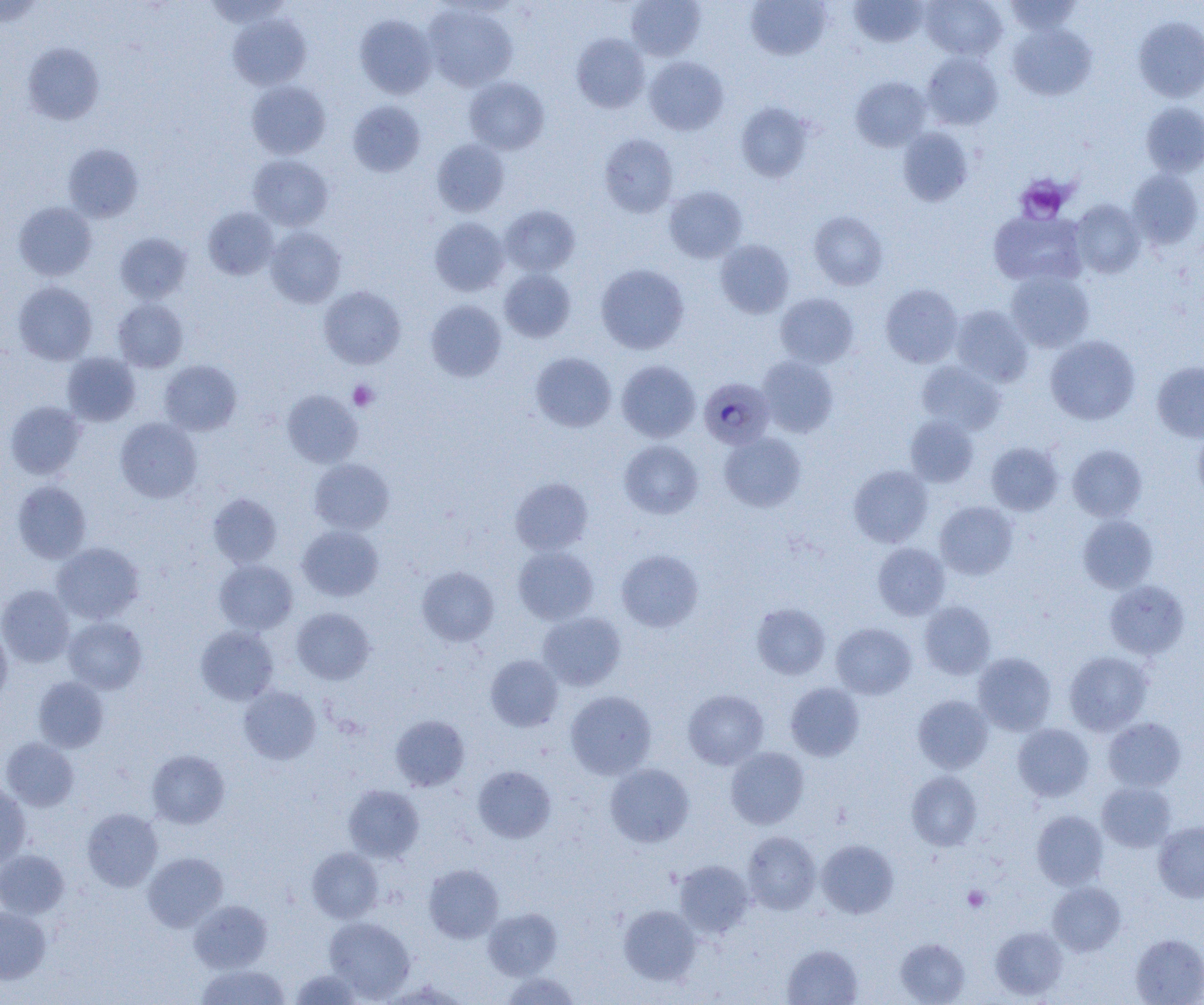
slide-level diagnosis = Plasmodium malariae
field of view = one of a larger specimen
image size = 1204×1005 pixels
magnification = 1000x
Plasmodium malariae-infected red blood cell locations = approximate bounding boxes as [x1, y1, x2, y2] in pixels: [699, 377, 775, 449]
modality = light microscopy
platelet locations = approximate bounding boxes as [x1, y1, x2, y2] in pixels: [1015, 174, 1073, 223], [348, 380, 378, 411], [962, 886, 990, 912]
preparation = thin blood smear
uninfected red blood cell locations = approximate bounding boxes as [x1, y1, x2, y2] in pixels: [626, 0, 706, 61], [849, 0, 927, 47], [921, 0, 1007, 60], [1004, 0, 1082, 34], [0, 1, 46, 27], [746, 1, 832, 61], [423, 4, 519, 92], [229, 13, 310, 91], [355, 14, 437, 99], [1134, 16, 1204, 102], [1008, 23, 1096, 100], [572, 33, 649, 113], [22, 43, 104, 125], [921, 52, 1003, 130], [644, 57, 728, 135], [464, 77, 549, 155], [851, 77, 931, 151], [246, 80, 330, 159], [347, 100, 425, 176], [1141, 102, 1204, 177], [736, 103, 813, 182], [898, 127, 973, 206], [599, 134, 679, 217], [432, 139, 509, 216], [62, 143, 144, 223], [248, 154, 333, 230], [1126, 169, 1203, 249], [664, 185, 747, 262], [1070, 200, 1145, 278], [14, 202, 97, 280], [500, 204, 580, 276], [203, 207, 279, 280], [989, 210, 1086, 286], [809, 211, 888, 290], [429, 217, 509, 296], [265, 225, 346, 308], [115, 232, 192, 303], [715, 239, 794, 318], [596, 264, 689, 354], [499, 268, 576, 342], [1005, 270, 1095, 352], [13, 281, 97, 365], [880, 284, 963, 367], [318, 286, 406, 369], [775, 292, 859, 368], [113, 298, 188, 372], [426, 300, 507, 382], [949, 305, 1034, 387], [1045, 335, 1140, 425], [62, 352, 141, 426], [531, 352, 616, 432], [757, 357, 838, 437], [159, 360, 241, 435], [617, 360, 701, 442], [915, 361, 1005, 435], [1151, 361, 1204, 442], [282, 390, 363, 468], [5, 401, 86, 480], [905, 415, 979, 487], [115, 417, 202, 503], [1192, 426, 1204, 505], [719, 432, 806, 511], [619, 440, 703, 519], [986, 442, 1063, 515], [1068, 444, 1147, 521], [309, 458, 394, 535], [848, 465, 933, 547], [510, 478, 593, 554], [12, 481, 91, 563], [208, 493, 282, 568], [935, 501, 1018, 580], [1078, 515, 1157, 593], [297, 525, 383, 601], [52, 542, 144, 624], [872, 542, 950, 620], [513, 546, 599, 625], [616, 549, 703, 632], [214, 559, 298, 634], [416, 566, 499, 646], [1105, 579, 1189, 659], [0, 585, 74, 667], [919, 601, 996, 679], [751, 603, 830, 679], [291, 608, 375, 684], [537, 612, 626, 690], [63, 617, 147, 693], [831, 623, 916, 699], [0, 625, 12, 704], [196, 625, 278, 705], [1064, 650, 1152, 735], [973, 652, 1056, 735], [485, 655, 563, 731], [33, 676, 109, 752], [785, 682, 864, 760], [239, 685, 321, 765], [683, 689, 769, 769], [565, 691, 656, 779], [913, 694, 993, 773], [390, 715, 469, 791], [1103, 717, 1186, 792], [1012, 723, 1094, 801], [1, 737, 79, 811], [725, 747, 809, 829], [147, 750, 229, 828], [605, 763, 694, 847], [473, 766, 556, 843], [907, 771, 982, 851], [1097, 781, 1177, 852], [0, 783, 31, 868], [344, 785, 424, 862], [82, 808, 163, 891], [1032, 810, 1107, 889], [1153, 821, 1204, 903], [742, 831, 821, 914], [816, 840, 898, 918], [307, 847, 383, 923], [0, 850, 69, 919], [142, 852, 227, 931], [675, 860, 754, 938], [424, 864, 503, 943], [1047, 881, 1126, 956], [189, 900, 272, 973], [618, 905, 700, 985], [0, 906, 51, 984], [482, 908, 562, 980], [324, 917, 415, 1002], [989, 925, 1067, 1000], [1131, 933, 1204, 1004], [895, 937, 970, 1004], [782, 944, 863, 1005], [196, 964, 290, 1005], [290, 969, 364, 1004], [500, 972, 581, 1004], [384, 980, 466, 1004]